Describe the morphology of the red blood cells.
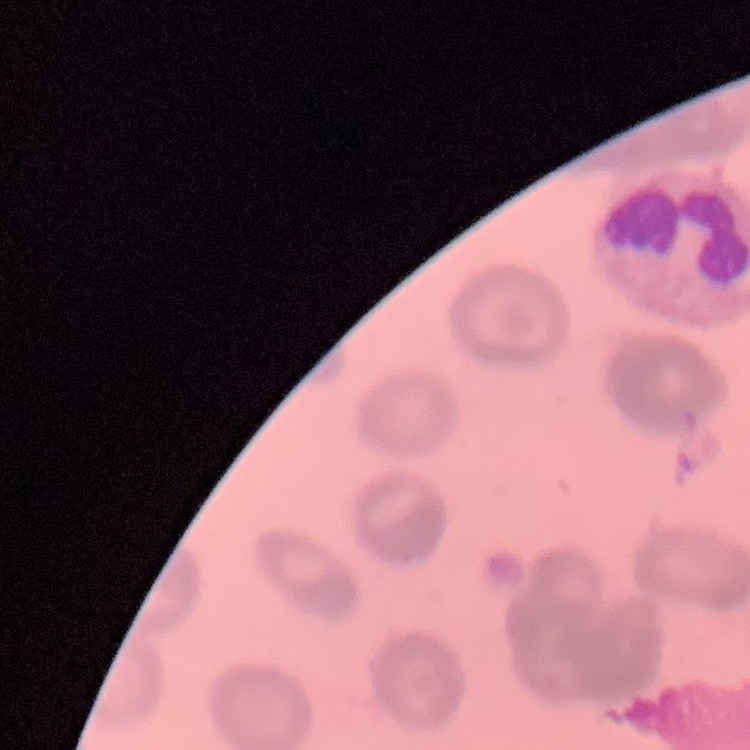

They show rouleaux formation.

preparation = thin blood film
stain = Field's or Giemsa
image type = square crop of a larger photomicrograph